Give the position of every Plasmodium parasite visible.
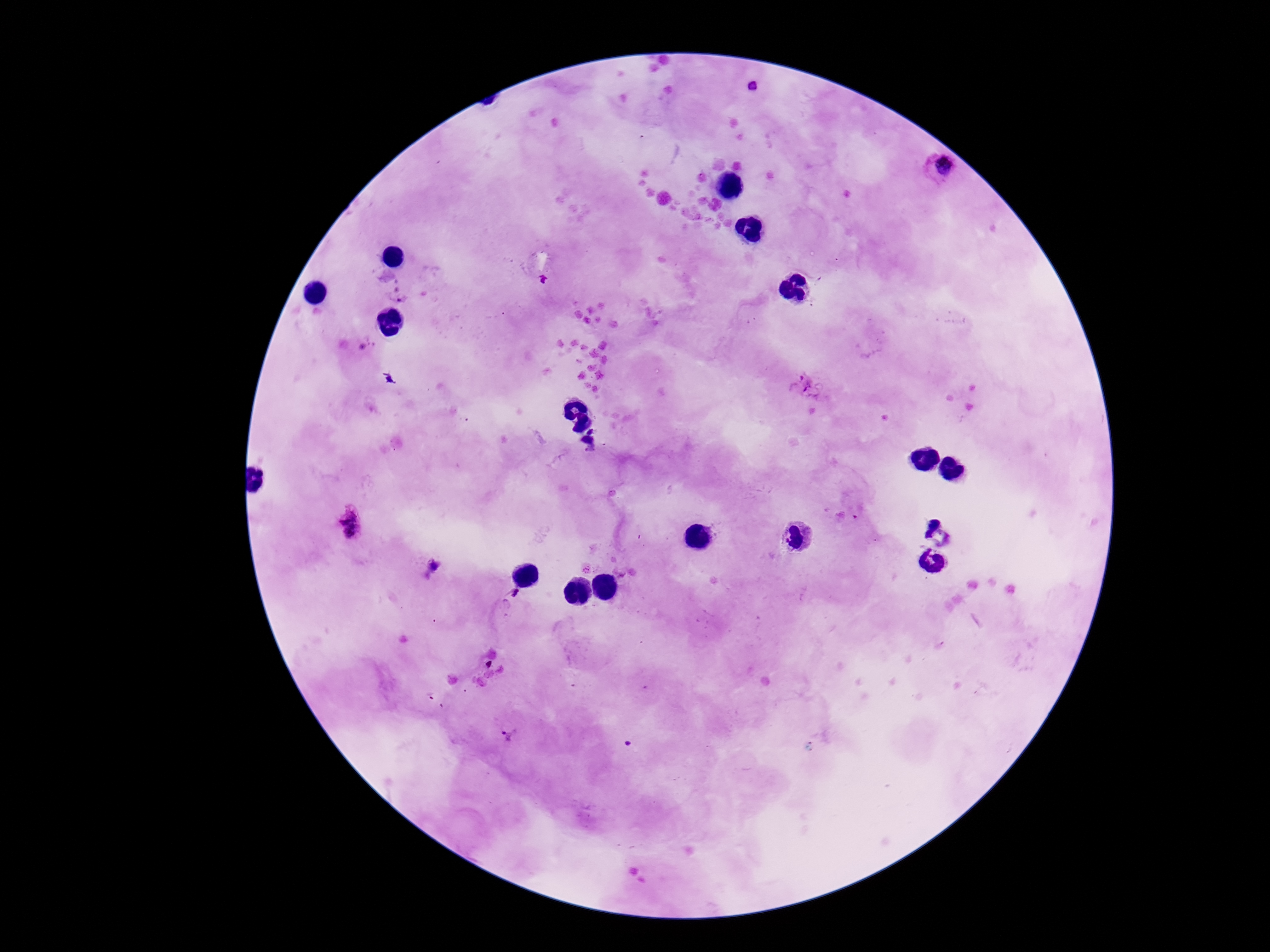
Approximate centers as (x, y) in pixels.
Plasmodium parasites: (752, 87), (936, 169), (400, 299), (365, 344), (805, 384), (592, 431), (585, 445), (351, 524), (586, 569), (510, 735).

Summary:
  - Stain: Giemsa
  - Patient malaria status: infected
  - Preparation: thick peripheral-blood smear
  - Capture: smartphone camera through the microscope eyepiece
  - Field of view: one from this slide
  - Image size: 1270×952 pixels
  - Magnification: 100x